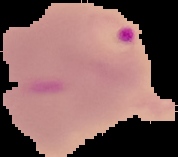

{
  "result": "malaria parasites detected",
  "image_size": "178×157 pixels",
  "preparation": "thin blood film",
  "image_type": "segmented cell region on a black background"
}